Describe the morphology of the erythrocytes.
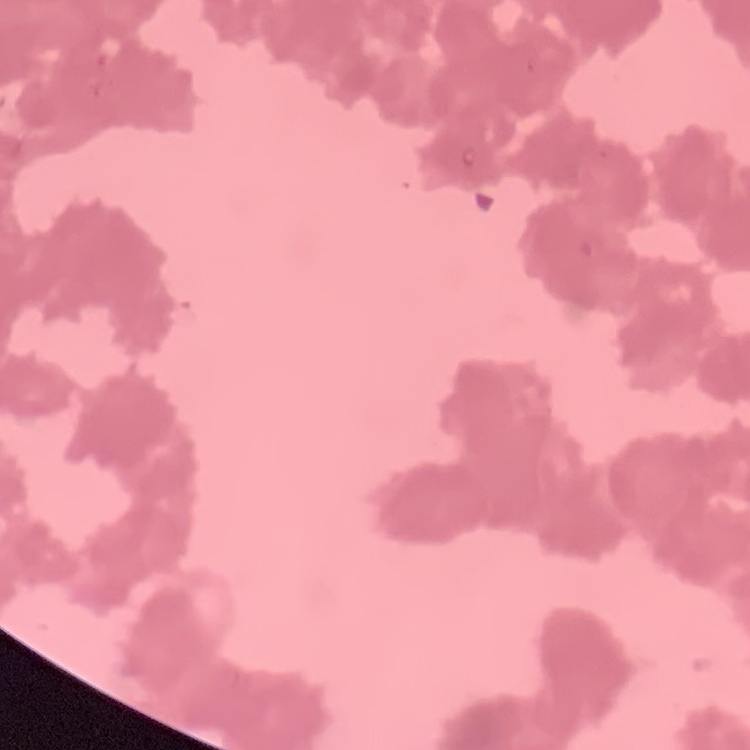
They show rouleaux formation.

Summary:
  - Preparation: thin blood film
  - Stain: Field's or Giemsa
  - Image type: one tile cut from a larger photomicrograph